State which parasite is depicted.
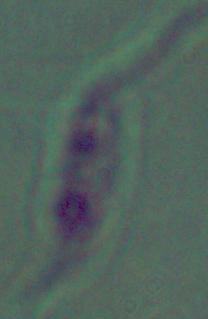

This is Leishmania.

magnification = 1000x
modality = micrograph